Give the preparation type.
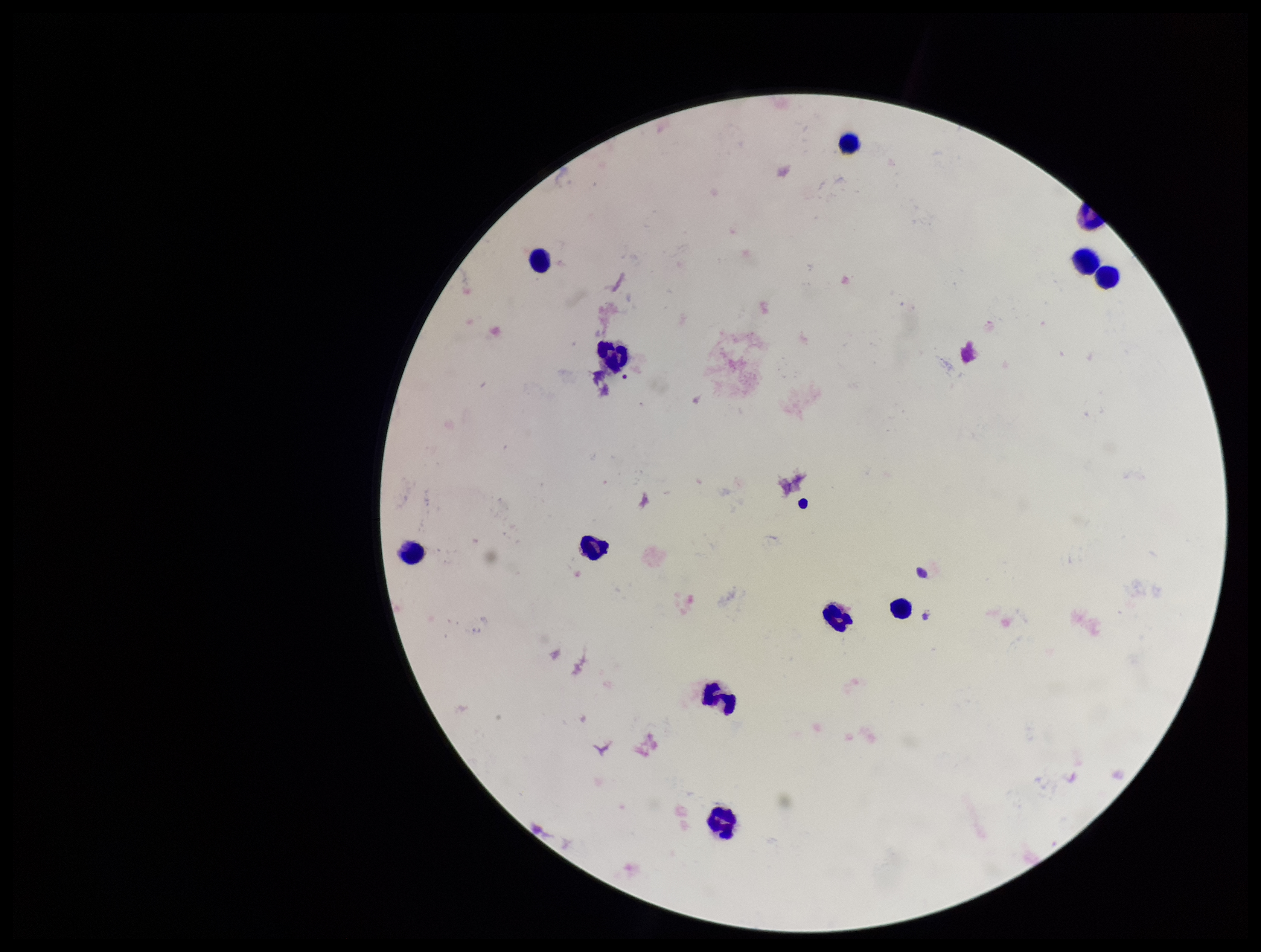
Thick.

Plasmodium parasites: none identified. Parasite count: 0. Patient malaria status: negative. One field from this slide. Giemsa stain. Image is 1261×952 pixels. Leukocyte count: 11. Smartphone photograph taken through the eyepiece of a microscope.